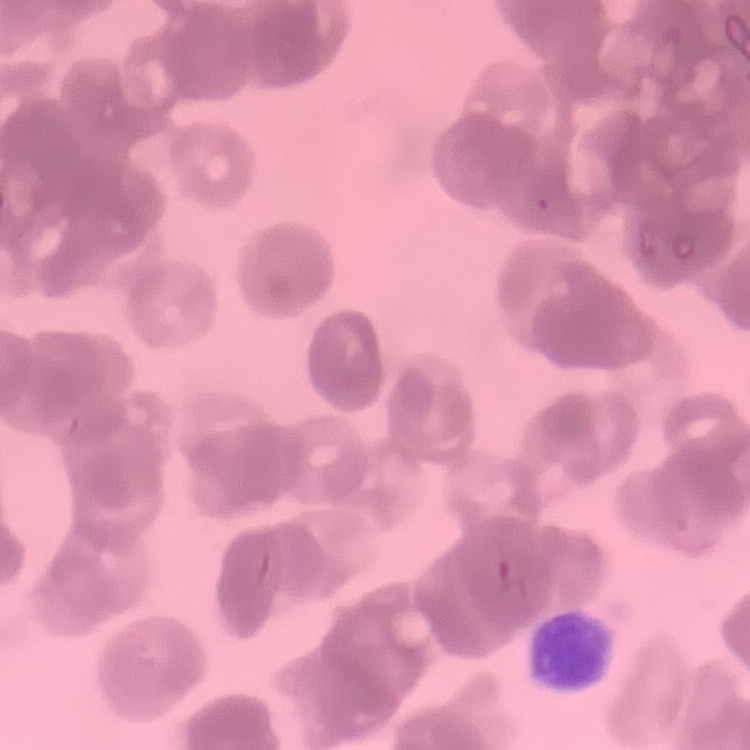

The red blood cells show rouleaux formation. Thin blood film. One tile cut from a larger photomicrograph. Stained with either Field's or Giemsa.